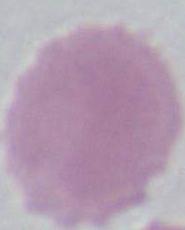
magnification = 1000x
modality = photomicrograph
identification = erythrocyte